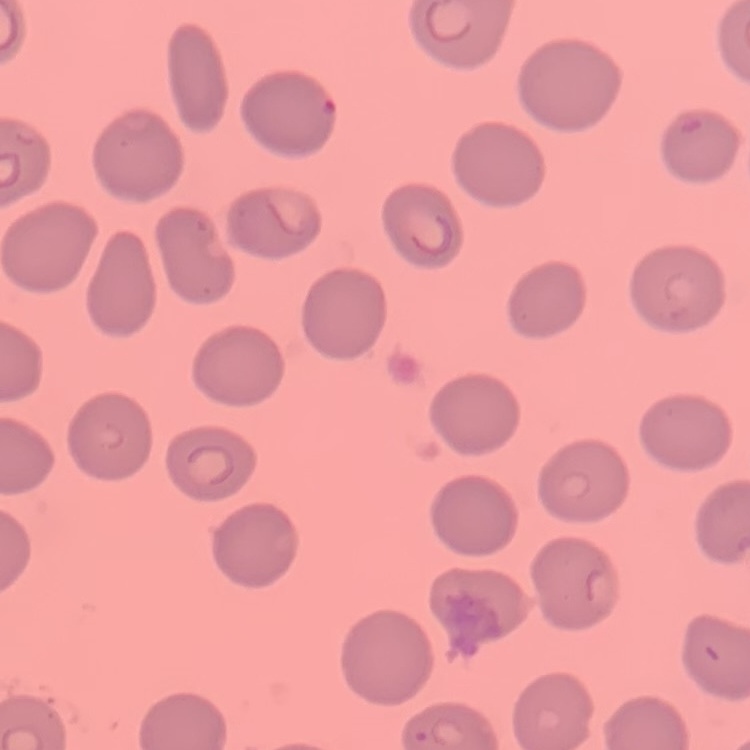
Summary:
  - Red blood cell morphology: no rouleaux formation
  - Stain: Field's or Giemsa
  - Preparation: thin blood film
  - Image type: one tile cut from a larger photomicrograph